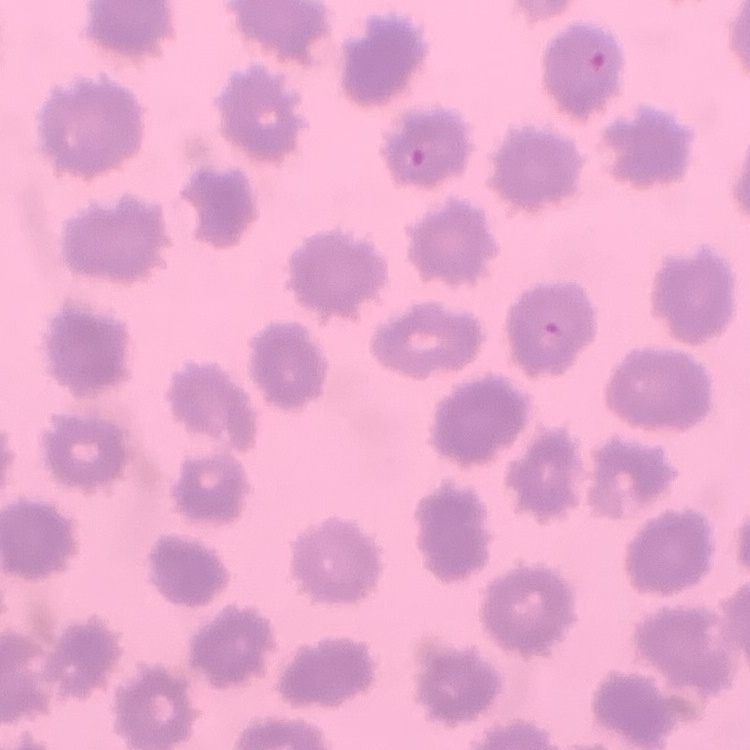

The red blood cells exhibit no rouleaux formation. Stained with either Field's or Giemsa. One tile cut from a larger photomicrograph. Thin blood film.